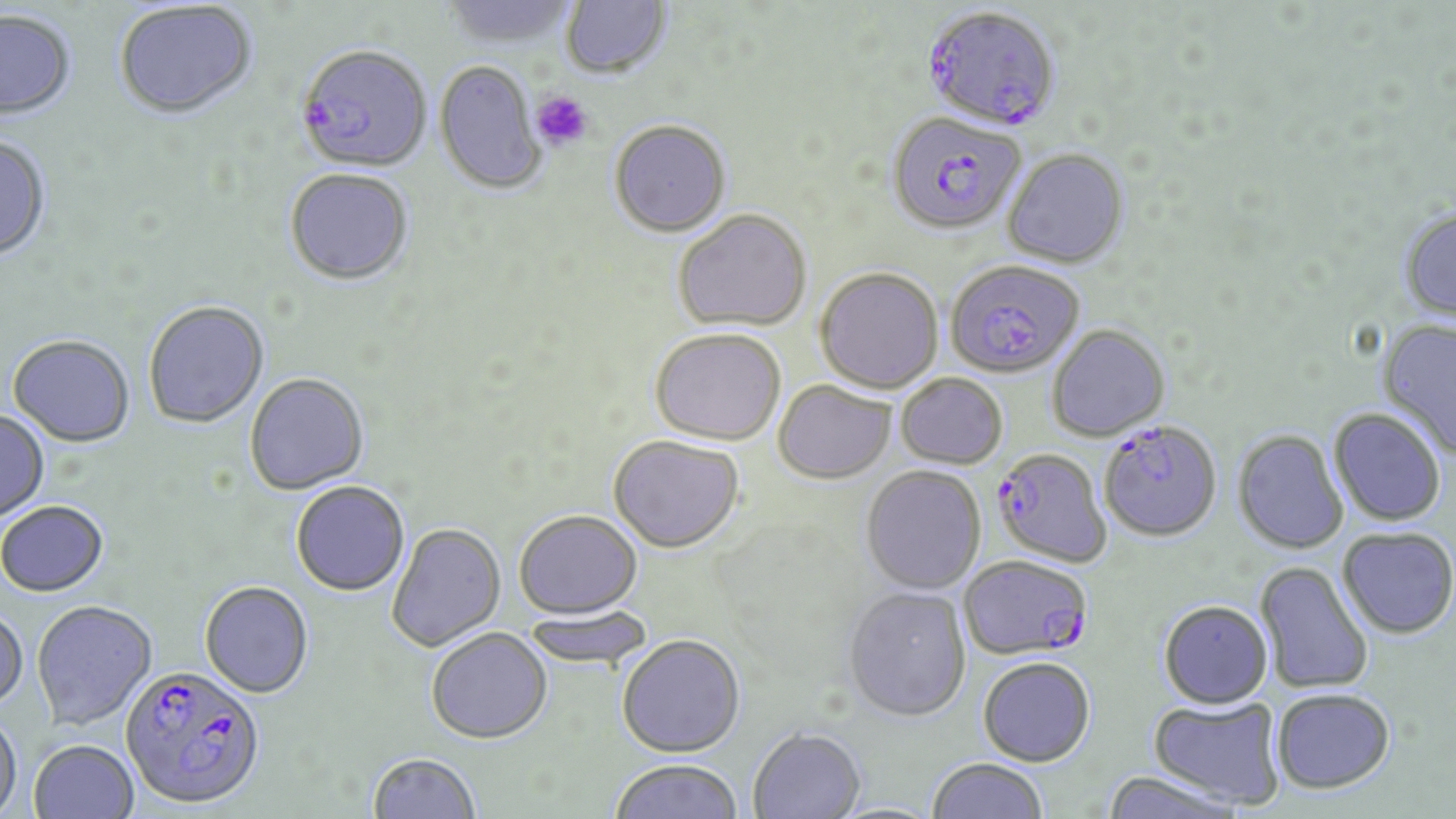

Summary:
  - Coordinate format: approximate bounding boxes as (x1, y1, x2, y2) in pixels
  - Platelet locations: (530, 89, 594, 151)
  - Uninfected red blood cell locations: (440, 0, 579, 50), (560, 0, 672, 81), (114, 3, 257, 123), (0, 11, 77, 122), (434, 60, 546, 195), (608, 119, 731, 236), (0, 137, 52, 264), (1002, 147, 1129, 268), (284, 171, 413, 288), (673, 208, 812, 331), (1400, 208, 1456, 322), (815, 266, 943, 394), (144, 302, 269, 430), (1377, 319, 1456, 459), (1047, 324, 1170, 442), (650, 327, 786, 445), (7, 337, 135, 450), (896, 372, 1008, 469), (244, 374, 369, 496), (773, 380, 895, 483), (1329, 408, 1446, 526), (0, 411, 49, 524), (1233, 429, 1349, 554), (608, 434, 745, 553), (861, 466, 986, 594), (291, 481, 410, 596), (0, 502, 109, 598), (513, 509, 642, 618), (386, 523, 506, 652), (1338, 526, 1456, 638), (1254, 560, 1375, 695), (199, 581, 314, 698), (843, 586, 971, 721), (1158, 599, 1273, 707), (32, 602, 158, 730), (520, 606, 655, 669), (0, 609, 28, 711), (425, 627, 553, 744), (616, 633, 745, 756), (977, 656, 1096, 766), (1270, 687, 1395, 794), (1148, 696, 1287, 810), (0, 713, 23, 819), (748, 727, 866, 819), (29, 741, 139, 819), (367, 751, 482, 818), (925, 757, 1049, 818), (608, 758, 743, 819), (1100, 770, 1247, 819)
  - Plasmodium falciparum-infected red blood cell locations: (925, 5, 1065, 131), (296, 48, 432, 176), (886, 111, 1026, 234), (945, 259, 1084, 378), (1098, 420, 1222, 541), (992, 447, 1112, 568), (959, 555, 1093, 660), (119, 666, 266, 810)
  - Slide-level diagnosis: Plasmodium falciparum
  - Stain: May-Grünwald-Giemsa
  - Magnification: 1000x
  - Modality: light microscopy
  - Field of view: one of a larger specimen
  - Preparation: thin blood film
  - Image size: 1456×819 pixels